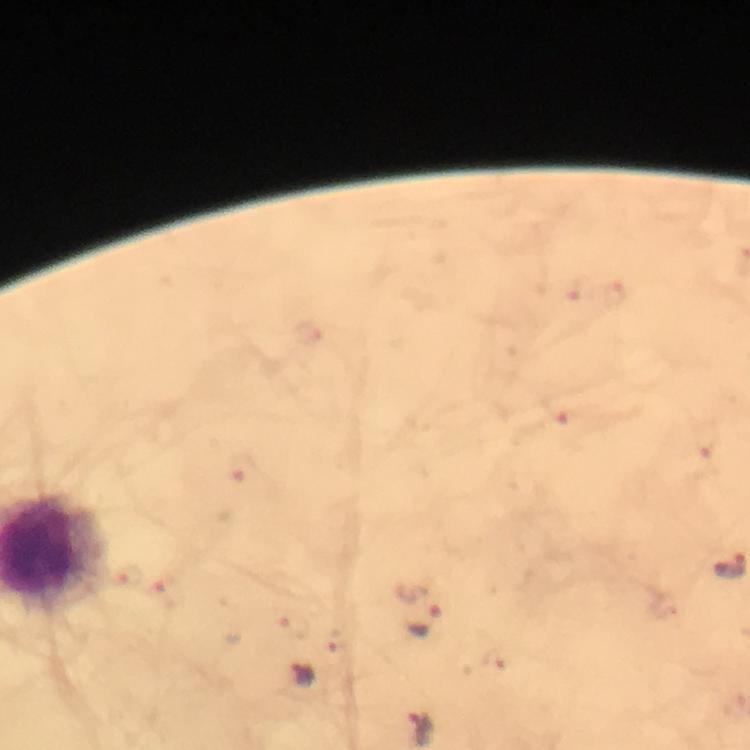
Approximate centers as (x, y) in pixels. Plasmodium parasite locations: (577, 288), (614, 295), (565, 409), (707, 445), (240, 471), (126, 575), (165, 592), (423, 620), (304, 675). 100x magnification. Giemsa stain. From a malaria diagnostic workup. Cropped region of a single field of view. Image is 750×750 pixels. Immersion oil was used. Smartphone photograph taken through a microscope. Thick smear.